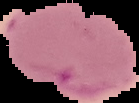

image type = segmented cell region on a black background
malaria status = parasitized
preparation = thin blood film
image size = 139×103 pixels